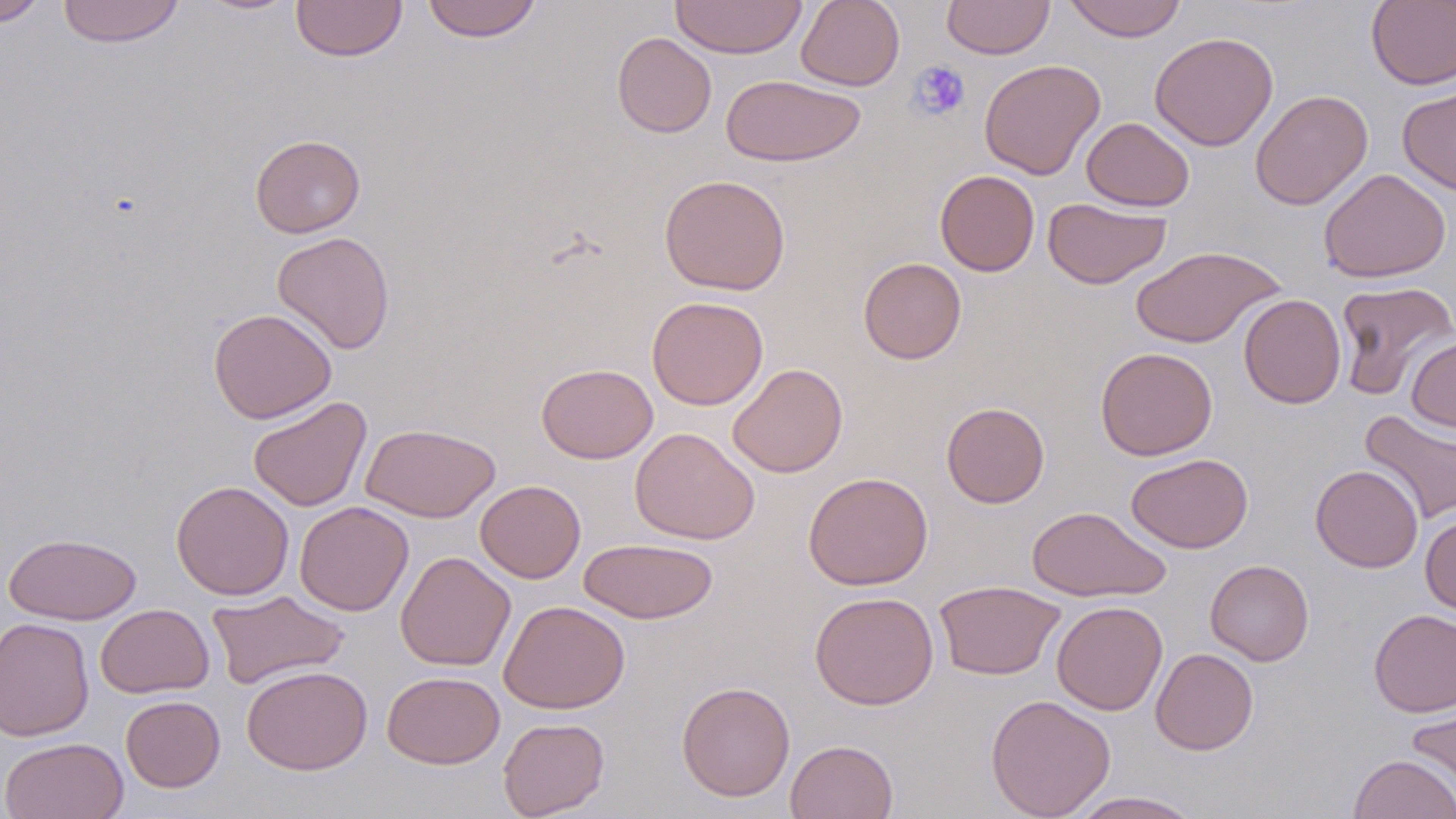
Summary:
  - Coordinate format: approximate bounding boxes as [x1, y1, x2, y2] in pixels
  - Uninfected red blood cell locations: [0, 0, 47, 26], [57, 0, 185, 48], [193, 0, 302, 15], [421, 0, 543, 42], [670, 0, 808, 59], [796, 0, 905, 91], [1064, 0, 1187, 42], [1366, 0, 1456, 90], [291, 1, 408, 62], [941, 1, 1054, 59], [612, 32, 716, 138], [1149, 32, 1278, 151], [979, 59, 1106, 180], [720, 74, 866, 166], [1397, 82, 1456, 196], [1250, 89, 1373, 210], [1081, 117, 1194, 212], [249, 134, 365, 238], [1318, 169, 1451, 283], [935, 170, 1040, 276], [659, 174, 791, 295], [1043, 197, 1171, 289], [271, 231, 396, 354], [1131, 245, 1285, 349], [858, 257, 966, 364], [1334, 280, 1456, 399], [1239, 294, 1346, 409], [646, 296, 769, 410], [208, 308, 337, 424], [1406, 337, 1456, 433], [1095, 347, 1218, 461], [536, 363, 658, 464], [728, 363, 848, 477], [247, 396, 372, 512], [941, 402, 1049, 508], [1359, 410, 1456, 524], [360, 423, 501, 522], [630, 427, 759, 544], [1126, 453, 1253, 553], [1310, 464, 1423, 572], [803, 471, 933, 590], [475, 479, 586, 583], [170, 480, 294, 600], [294, 501, 414, 616], [1027, 506, 1170, 601], [1420, 514, 1456, 617], [2, 532, 141, 625], [579, 537, 719, 624], [396, 551, 516, 671], [1205, 559, 1314, 665], [934, 580, 1066, 681], [207, 589, 349, 690], [809, 591, 939, 710], [499, 600, 630, 714], [1051, 600, 1168, 715], [95, 603, 214, 698], [1369, 608, 1456, 717], [0, 616, 95, 742], [1150, 648, 1258, 755], [241, 665, 372, 775], [382, 671, 505, 769], [677, 681, 795, 801], [985, 694, 1116, 819], [121, 695, 225, 792], [1406, 698, 1456, 810], [497, 717, 610, 818], [1, 737, 129, 819], [785, 739, 898, 819], [1348, 753, 1455, 818], [1066, 790, 1204, 819]
  - Platelet locations: [908, 60, 971, 120]
  - Slide-level diagnosis: negative for blood parasites
  - Magnification: 1000x
  - Modality: light microscopy
  - Image size: 1456×819 pixels
  - Stain: May-Grünwald-Giemsa
  - Preparation: thin blood smear
  - Field of view: one of a larger specimen